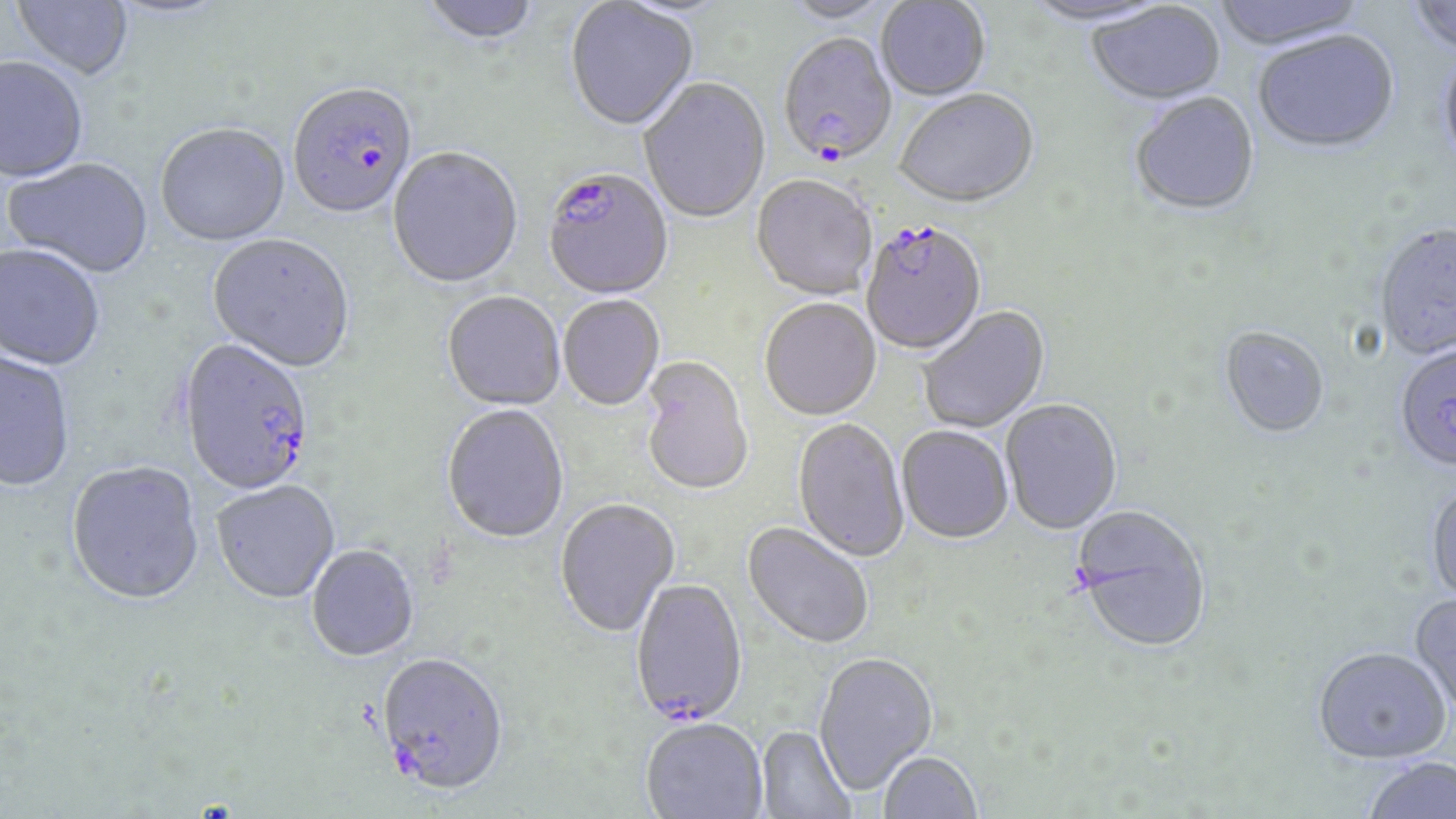

slide-level diagnosis = Plasmodium falciparum
field of view = single
image size = 1456×819 pixels
Plasmodium falciparum-infected red blood cell locations = approximate bounding boxes as (x1, y1, x2, y2) in pixels: (778, 36, 898, 169), (288, 85, 419, 222), (543, 171, 674, 302), (865, 219, 984, 355), (179, 341, 314, 498), (629, 579, 748, 730), (376, 656, 508, 800)
preparation = thin blood smear
uninfected red blood cell locations = approximate bounding boxes as (x1, y1, x2, y2) in pixels: (11, 0, 134, 82), (876, 0, 990, 102), (1211, 0, 1370, 53), (1407, 0, 1456, 60), (420, 1, 542, 47), (780, 1, 898, 26), (1023, 1, 1175, 29), (564, 2, 699, 134), (1088, 3, 1226, 107), (1253, 33, 1399, 156), (1438, 51, 1456, 176), (0, 59, 88, 184), (638, 79, 771, 224), (895, 90, 1040, 211), (1130, 94, 1261, 218), (155, 126, 290, 249), (387, 149, 523, 291), (4, 159, 154, 281), (751, 177, 877, 302), (1374, 225, 1456, 362), (207, 236, 355, 375), (0, 246, 105, 373), (442, 293, 565, 412), (558, 296, 665, 412), (760, 300, 881, 422), (918, 306, 1051, 434), (1218, 327, 1329, 441), (0, 349, 76, 494), (1399, 349, 1456, 479), (639, 357, 754, 498), (1001, 400, 1122, 536), (442, 406, 569, 545), (792, 419, 909, 564), (896, 427, 1013, 546), (66, 463, 205, 609), (1425, 481, 1456, 607), (212, 482, 340, 605), (555, 499, 681, 639), (1071, 507, 1213, 657), (741, 523, 873, 651), (306, 546, 420, 664), (1408, 592, 1456, 716), (1312, 648, 1451, 766), (813, 654, 938, 797), (641, 721, 767, 819), (756, 727, 854, 819), (879, 753, 982, 819), (1363, 756, 1456, 819)
stain = May-Grünwald-Giemsa
modality = optical microscopy
magnification = 1000x